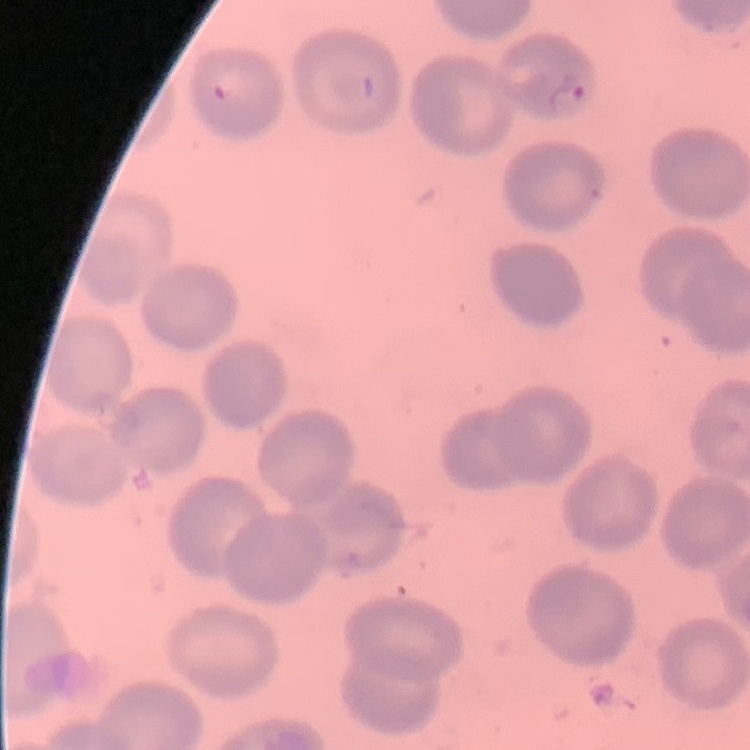

red blood cell morphology = no rouleaux formation
image type = one tile cut from a larger photomicrograph
preparation = thin blood smear
stain = Field's or Giemsa